Give the position of every Plasmodium parasite visible.
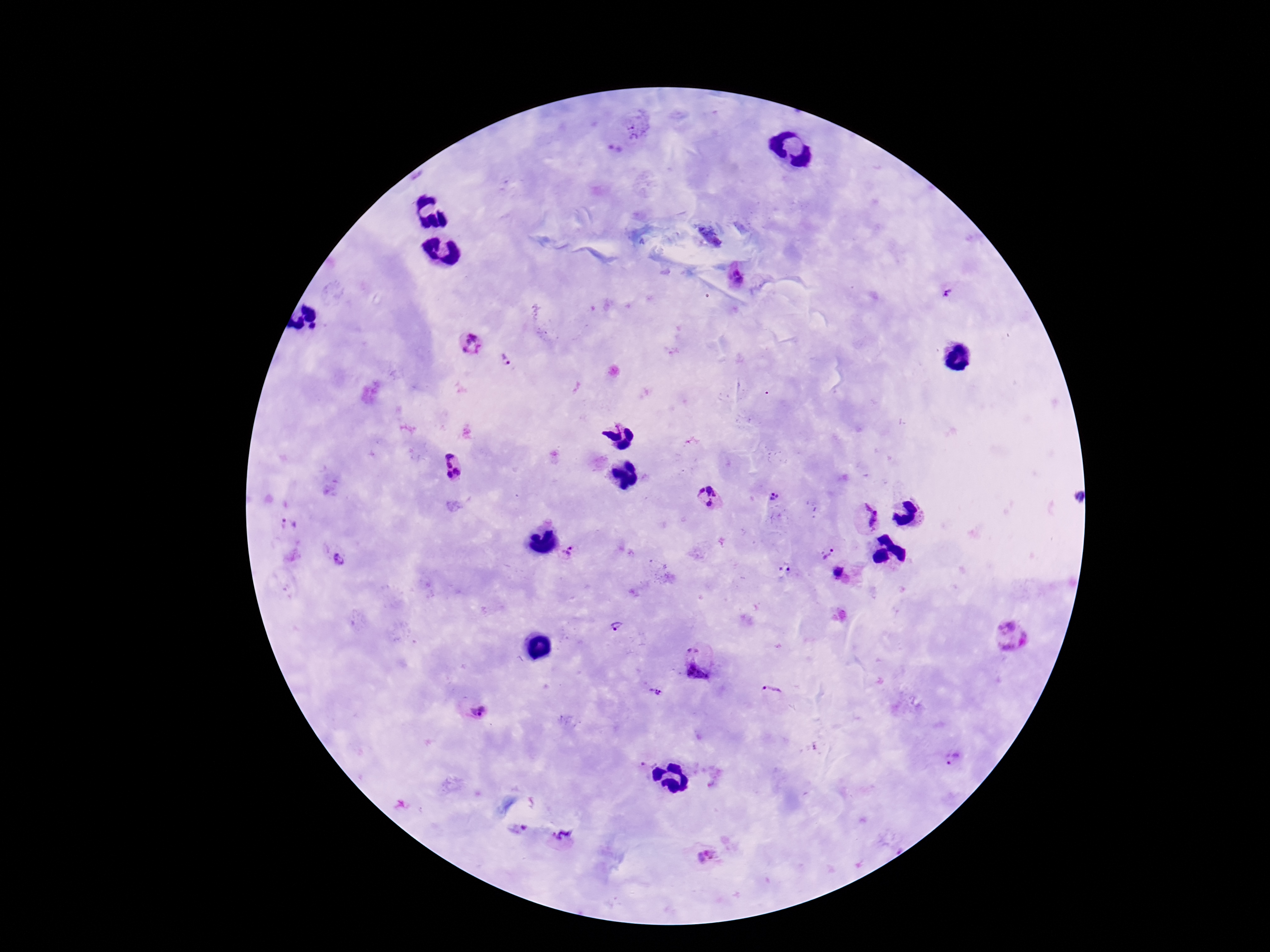

Approximate centers as (x, y) in pixels.
Plasmodium parasites: (637, 128), (734, 278), (946, 292), (471, 345), (507, 360), (451, 468), (773, 497), (708, 498), (866, 517), (288, 523), (569, 551), (826, 555), (339, 560), (785, 568), (838, 573), (616, 627), (1010, 638), (698, 662), (656, 691), (771, 691), (473, 709), (649, 758), (953, 758), (564, 838), (706, 855).

Summary:
  - Preparation: thick peripheral-blood smear
  - Field of view: one from this slide
  - Stain: Giemsa
  - Capture: smartphone camera through the microscope eyepiece
  - Image size: 1270×952 pixels
  - Magnification: 100x
  - Patient malaria status: infected